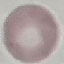

Summary:
  - Malaria status: uninfected
  - Stain: Giemsa
  - Image type: cell patch, automatically extracted from a larger field of view and resized to 64 × 64 pixels
  - Preparation: thin smear
  - Capture: smartphone camera at the microscope eyepiece